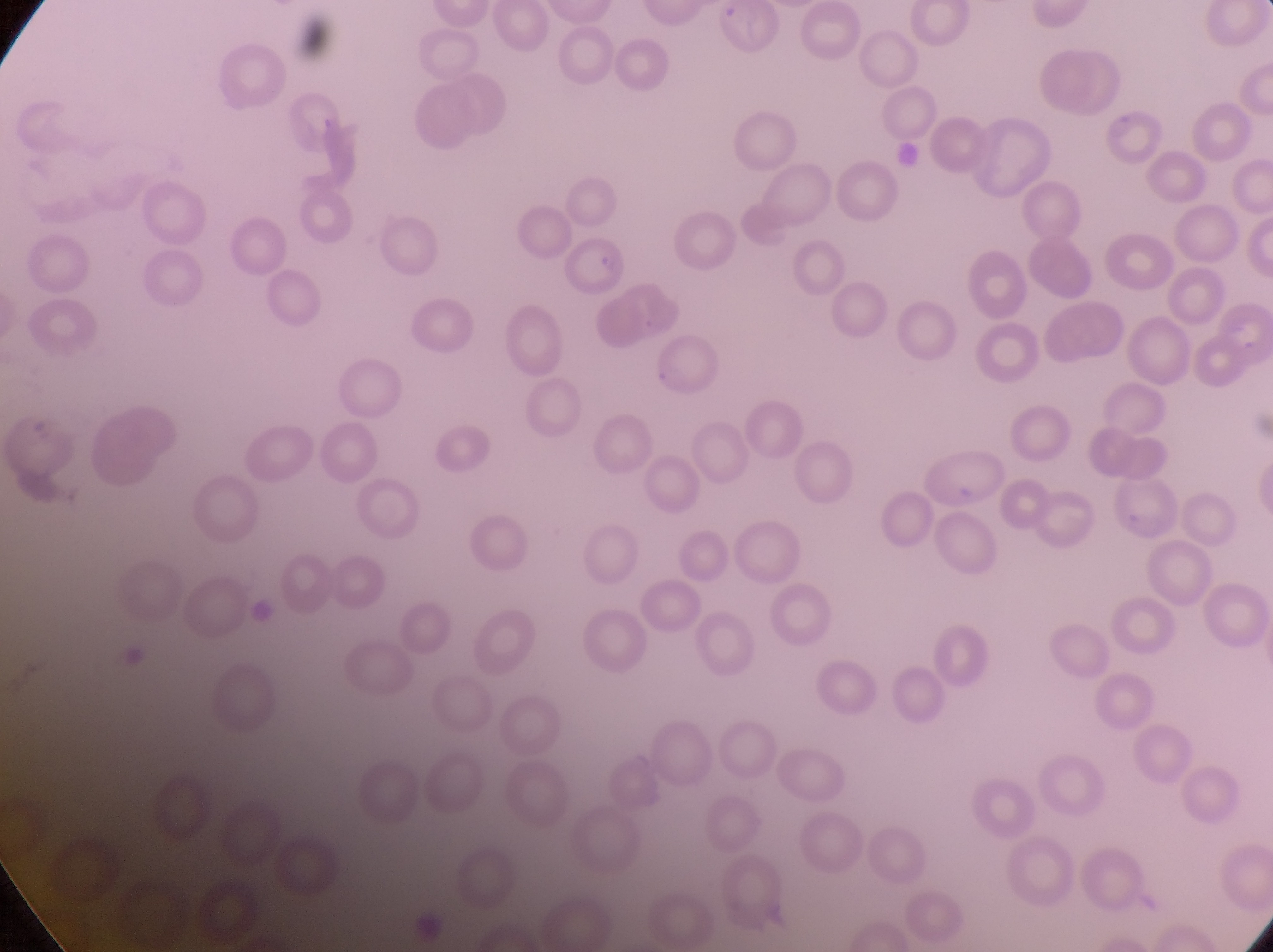

Approximate bounding boxes as left top right bottom in pixels.
Summary:
  - Parasitised red blood cell locations: 557 235 632 302
  - Preparation: thin blood smear
  - Country: Uganda
  - Magnification: 1000x
  - Image size: 1273×952 pixels
  - Capture: smartphone photograph through the eyepiece of an Olympus CX-23 microscope
  - Field of view: single